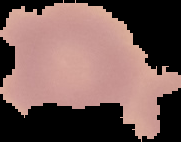

malaria status = uninfected
image type = segmented cell region on a black background
preparation = thin blood film
image size = 181×142 pixels